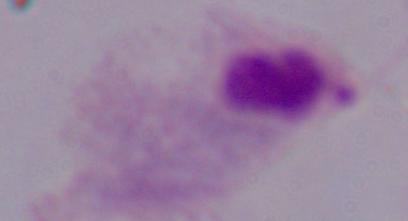

Captured at 1000x magnification. A trichomonad is seen. Photomicrograph.